Classify this cell by malaria status.
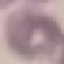
Uninfected.

Summary:
  - Preparation: thin blood smear
  - Image type: cell patch, automatically extracted from a larger field of view and resized to 64 × 64 pixels
  - Stain: Giemsa
  - Capture: smartphone camera at the microscope eyepiece